Give the position of every malaria parasite.
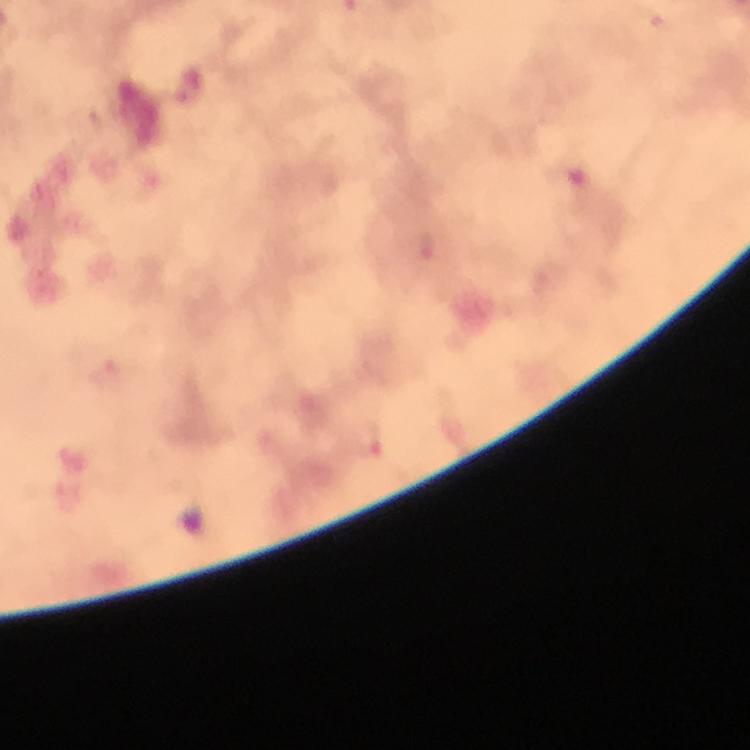
Approximate centers as (x, y) in pixels.
Malaria parasites: (652, 19), (428, 246), (109, 375), (366, 440).

Smartphone photograph taken through a microscope. A crop from one field of view. 100x magnification. Image is 750×750 pixels. Giemsa stain. Thick smear. From a diagnostic examination for malaria. Immersion oil was used.